Classify this cell by malaria status.
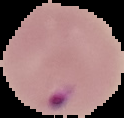

It is parasitized.

Segmented cell region on a black background. Image is 124×118 pixels. From a thin blood smear.